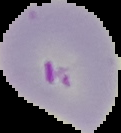 Result: malaria parasites detected. The area outside the segmented cell region is set to black. From a thin blood film. Image is 121×133 pixels.